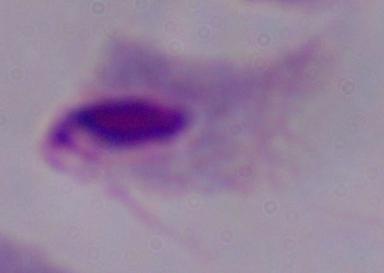

modality = micrograph
magnification = 1000x
identification = trichomonad